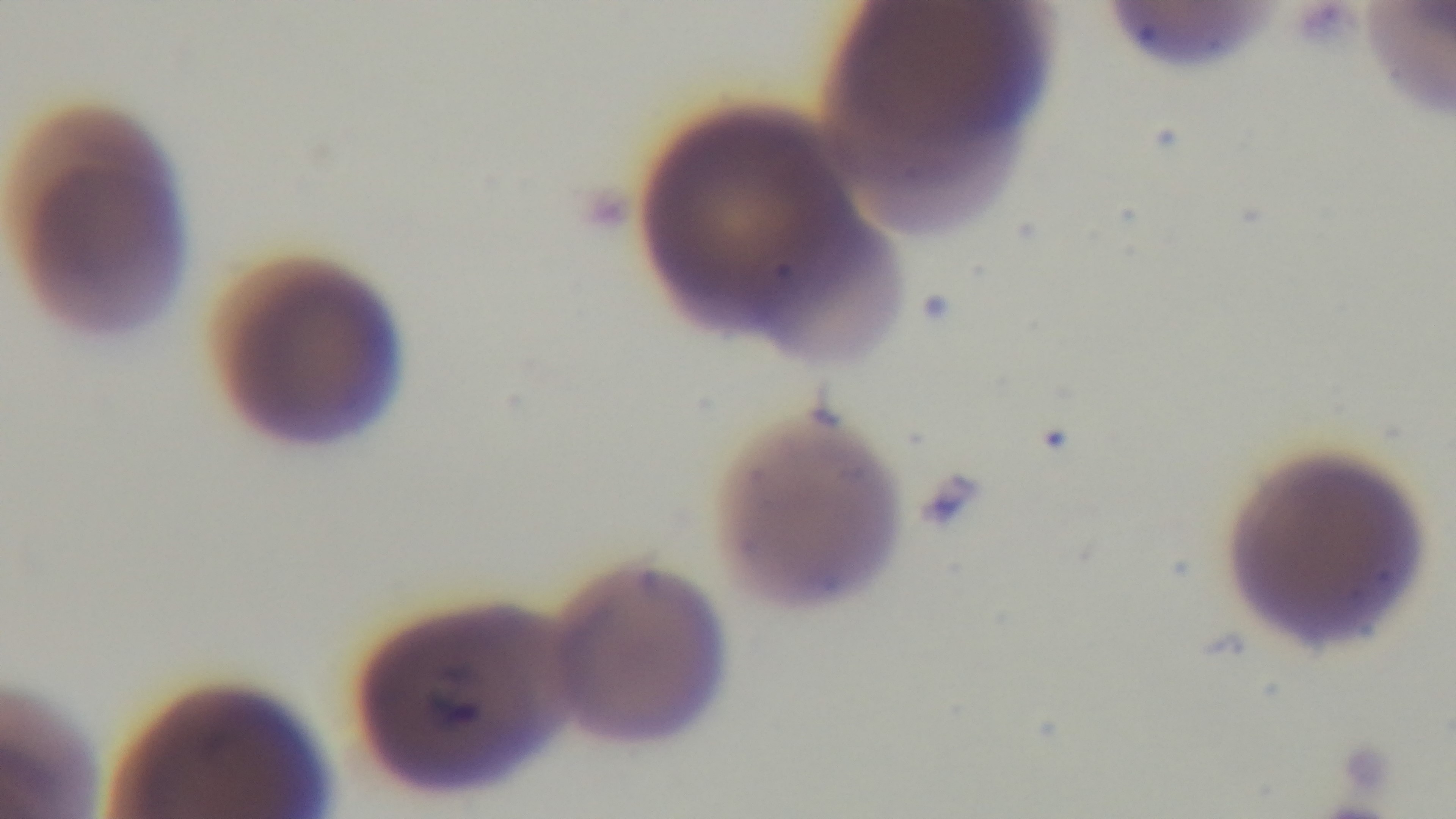
malaria status = infected
capture = mounted 4K digital camera
field of view = single
preparation = thin
objective = 100x oil immersion
stain = Giemsa
modality = light microscopy